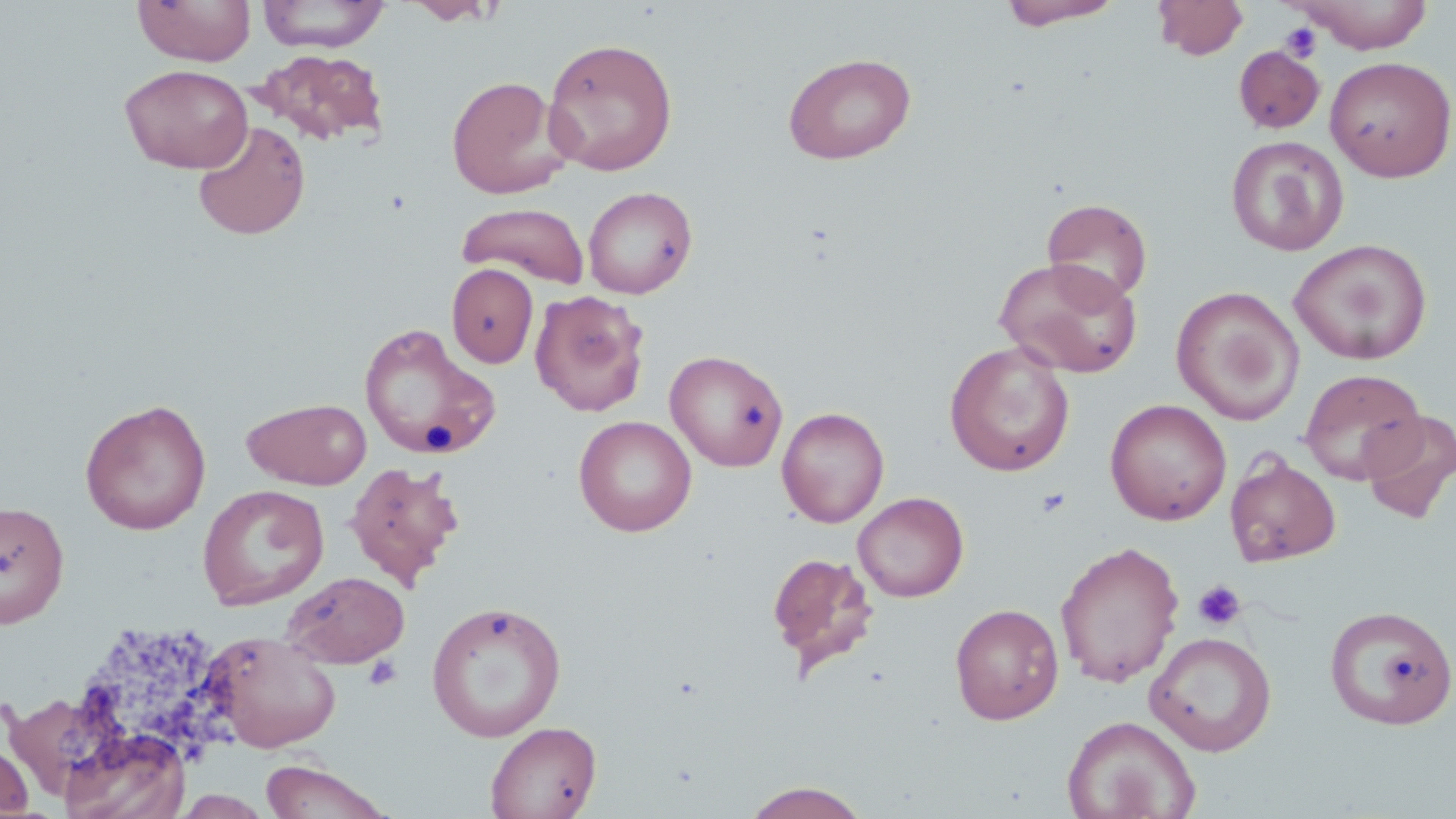

Approximate bounding boxes as (x1,y1)-(x2,y2) corner pairs in pixels. Uninfected red blood cell locations: (257,0)-(390,52), (404,0)-(501,25), (998,0)-(1126,30), (1153,0)-(1250,60), (1292,0)-(1435,54), (133,1)-(255,66), (542,37)-(679,176), (1233,45)-(1325,134), (253,48)-(388,147), (782,51)-(916,164), (1325,55)-(1456,182), (120,64)-(253,174), (446,76)-(570,199), (192,120)-(310,240), (1226,135)-(1350,256), (583,185)-(697,299), (1041,198)-(1152,306), (456,202)-(590,288), (1288,239)-(1432,365), (993,256)-(1144,379), (446,263)-(538,368), (1171,286)-(1304,425), (530,289)-(651,417), (359,322)-(501,460), (944,341)-(1075,477), (664,349)-(788,472), (1298,368)-(1427,485), (242,397)-(372,489), (79,398)-(212,535), (1105,398)-(1231,525), (776,406)-(890,527), (1359,409)-(1456,526), (573,415)-(697,537), (1225,452)-(1341,567), (345,460)-(465,590), (197,484)-(329,610), (853,491)-(969,602), (0,500)-(70,628), (1055,539)-(1185,688), (766,551)-(880,679), (283,571)-(409,668), (426,600)-(567,742), (949,603)-(1064,724), (1325,605)-(1456,729), (204,631)-(343,753), (1144,631)-(1277,756), (1062,714)-(1200,819), (484,720)-(601,819), (58,728)-(191,819), (0,736)-(35,817), (258,759)-(396,819), (740,780)-(873,818). Platelet locations: (1280,22)-(1324,62), (1035,487)-(1072,518), (1192,580)-(1247,631), (363,654)-(402,691). Slide-level diagnosis: negative for blood parasites. Captured at 1000x magnification. May-Grünwald-Giemsa stain. Thin blood smear. Optical microscopy. Single field of view. Image is 1456×819 pixels.